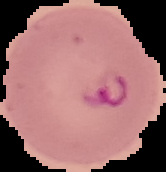
Summary:
  - Image size: 166×172 pixels
  - Image type: cell region segmented out of the field of view; surrounding area masked to black
  - Result: malaria parasites detected
  - Preparation: thin blood smear